Comment on the morphology of the red blood cells.
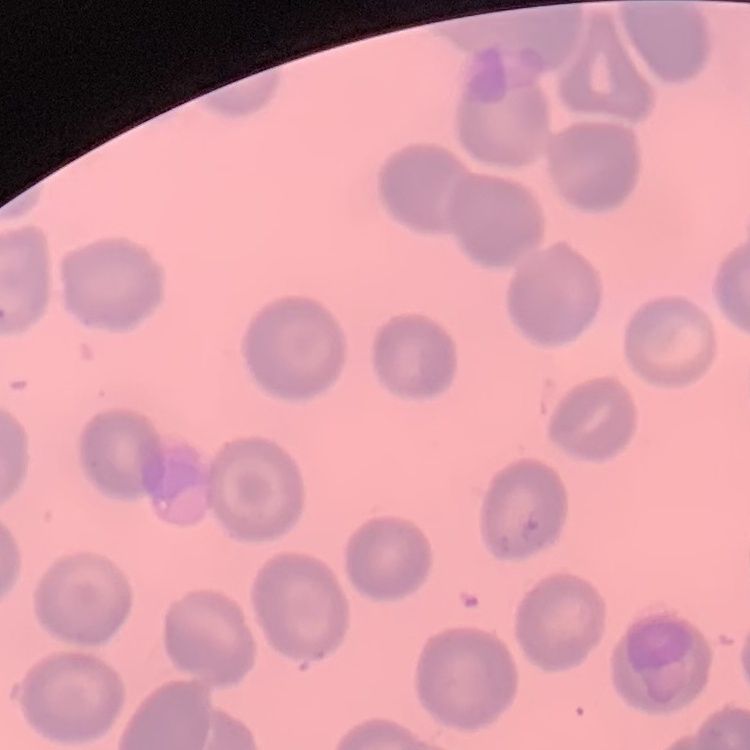

No rouleaux formation.

preparation = thin blood film
image type = one tile cut from a larger photomicrograph
stain = Field's or Giemsa